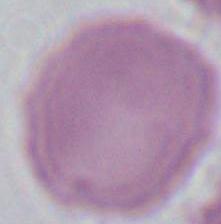
An erythrocyte is seen. Captured at 1000x magnification. Photomicrograph.